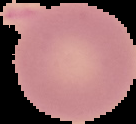
{
  "preparation": "thin blood film",
  "result": "negative for malaria parasites",
  "image_type": "segmented cell region with the area outside set to black",
  "image_size": "136×124 pixels"
}